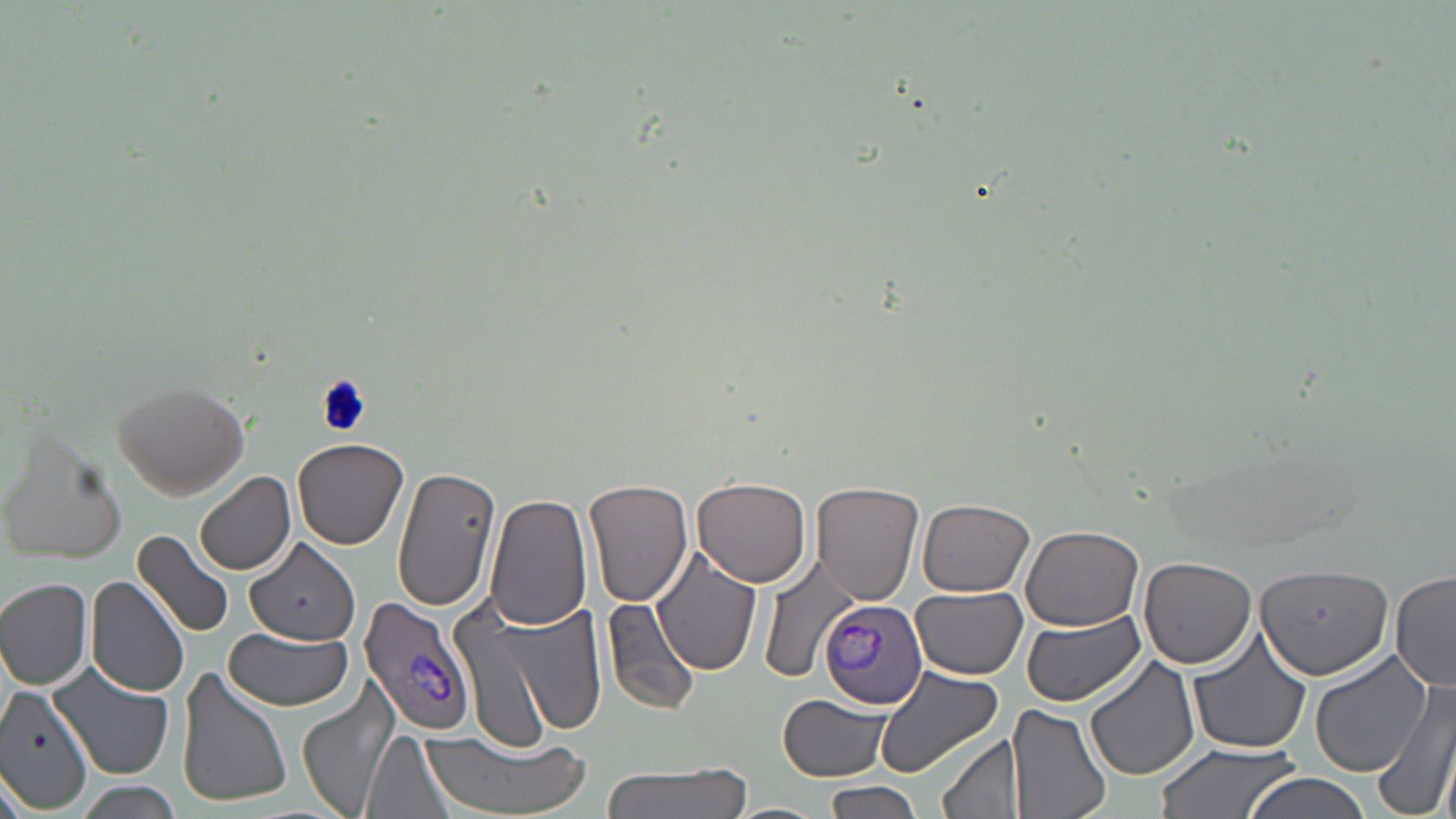
slide_level_diagnosis: Plasmodium vivax
preparation: thin blood film
stain: May-Grünwald-Giemsa
magnification: 1000x
plasmodium_vivax_infected_red_blood_cell_locations: 'approximate bounding boxes as [x1, y1, x2, y2] in pixels: [361, 595, 474, 736], [819, 598, 926, 711]'
image_size: 1456×819 pixels
field_of_view: single
uninfected_red_blood_cell_locations: 'approximate bounding boxes as [x1, y1, x2, y2] in pixels: [110, 379, 251, 498], [2, 428, 130, 567], [293, 436, 411, 549], [390, 465, 502, 614], [195, 472, 297, 577], [693, 476, 813, 584], [585, 479, 694, 608], [811, 481, 925, 606], [485, 493, 592, 632], [917, 498, 1035, 596], [1021, 525, 1147, 630], [134, 531, 238, 640], [244, 539, 362, 645], [653, 549, 763, 676], [758, 553, 861, 682], [1140, 556, 1256, 669], [1254, 561, 1397, 677], [1390, 570, 1455, 690], [88, 576, 189, 698], [1, 577, 95, 690], [910, 587, 1029, 679], [448, 591, 610, 746], [602, 599, 704, 717], [1022, 612, 1144, 706], [224, 626, 356, 712], [1185, 628, 1314, 753], [1307, 647, 1437, 777], [1082, 655, 1199, 783], [48, 664, 176, 779], [873, 664, 1006, 784], [176, 668, 291, 809], [298, 678, 396, 814], [1373, 680, 1456, 819], [0, 687, 97, 810], [778, 696, 893, 779], [1006, 703, 1113, 819], [363, 730, 460, 819], [419, 731, 590, 819], [939, 733, 1023, 819], [1153, 741, 1300, 818], [599, 759, 752, 819], [1242, 773, 1375, 819], [70, 780, 187, 819], [820, 782, 926, 819], [722, 802, 830, 819]'
modality: light microscopy